Name the parasite shown.
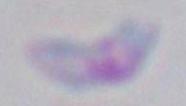

This is Toxoplasma gondii.

Summary:
  - Modality: micrograph
  - Magnification: 1000x